Evaluate for Plasmodium parasites.
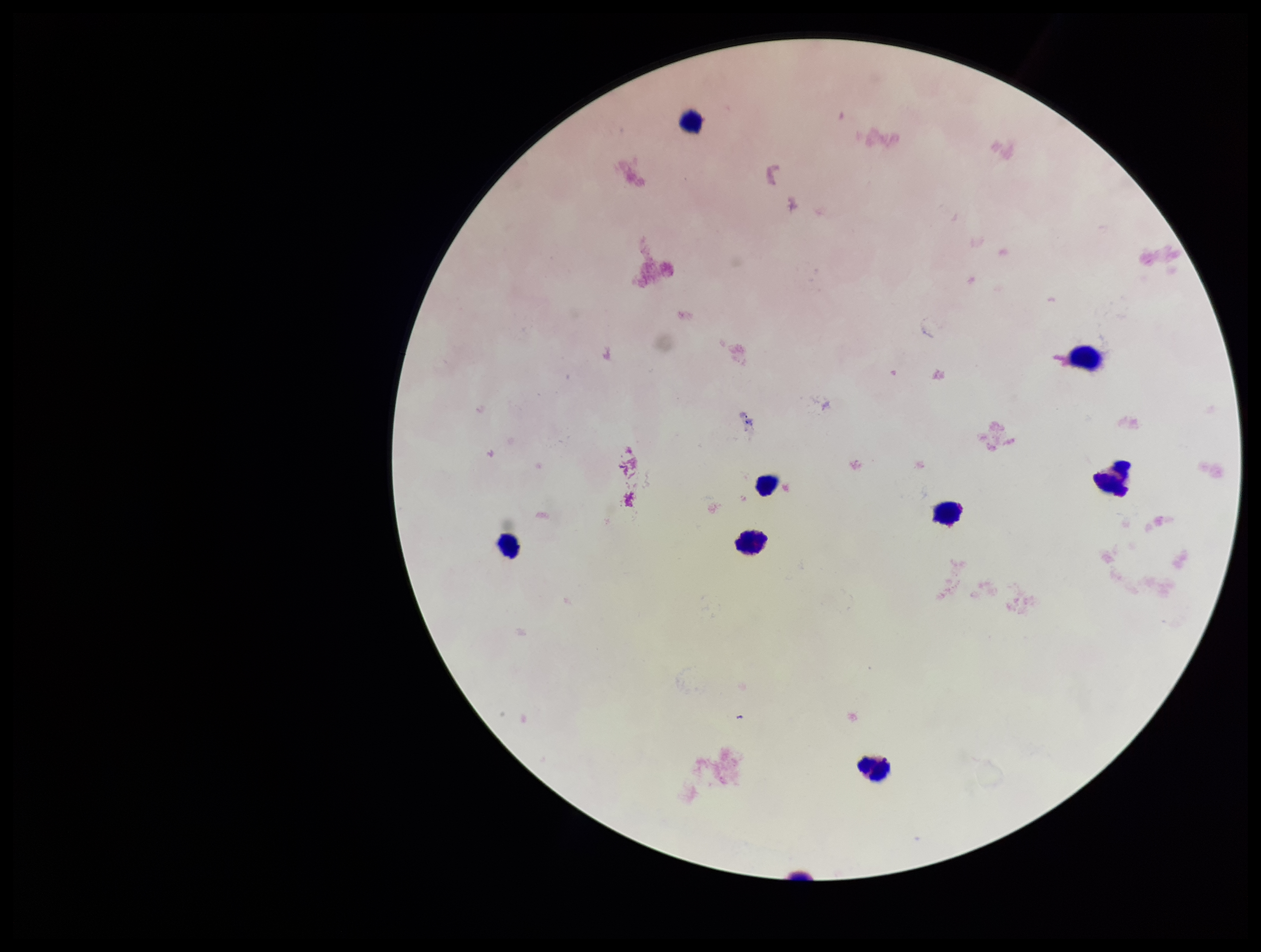
None detected.

Summary:
  - Leukocyte count: 8
  - Capture: smartphone photograph through the microscope eyepiece
  - Patient malaria status: negative
  - Image size: 1261×952 pixels
  - Field of view: single
  - Parasite count: 0
  - Stain: Giemsa
  - Preparation: thick